State which parasite is depicted.
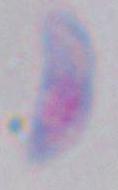

This is Toxoplasma gondii.

Summary:
  - Magnification: 1000x
  - Modality: micrograph